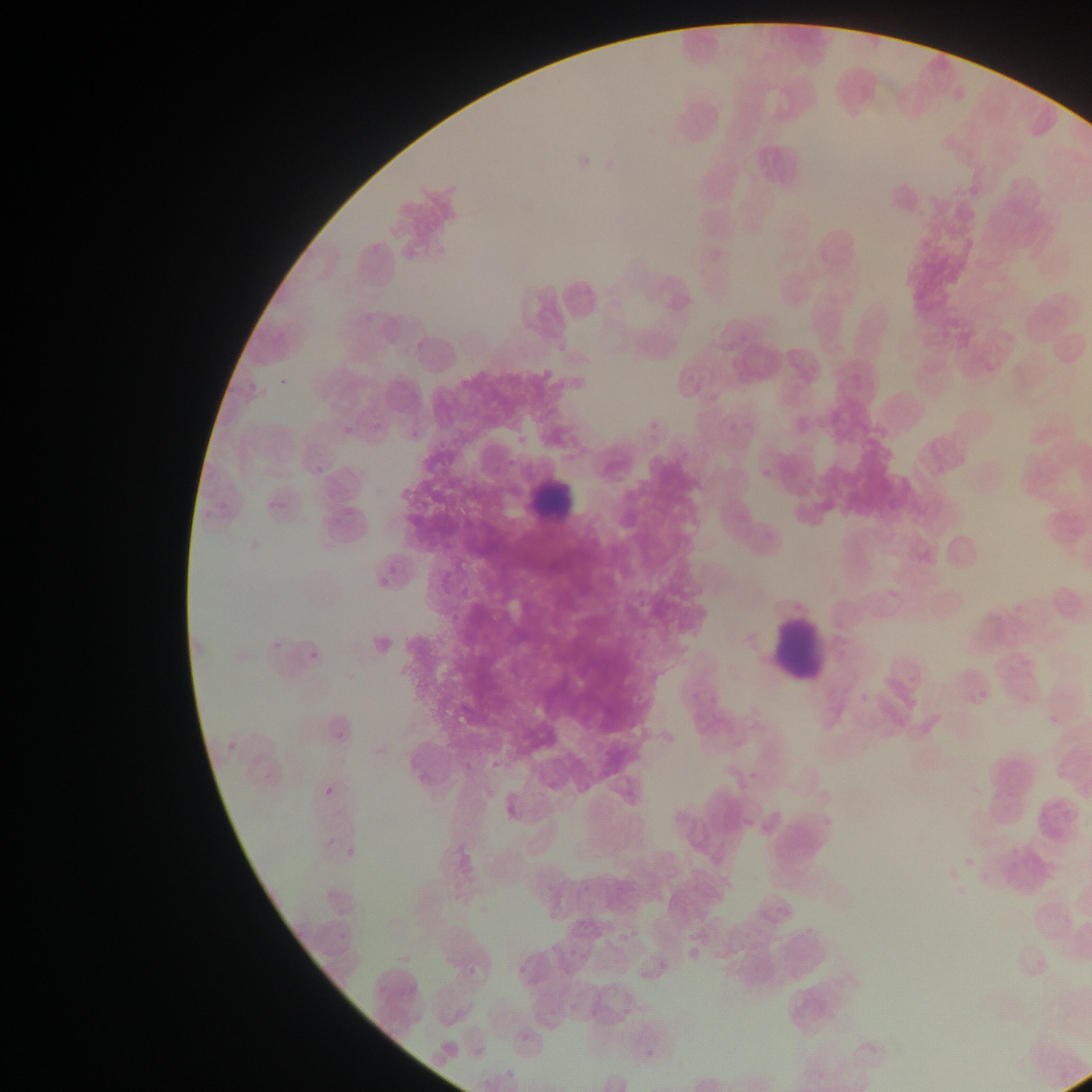 Approximate bounding boxes as [left, top, right, bottom] in pixels. Leukocyte locations: [663, 84, 730, 150], [526, 469, 594, 527], [762, 602, 832, 686]. Malaria parasite locations: [275, 368, 290, 387], [527, 368, 552, 388], [327, 409, 352, 434], [308, 450, 332, 474], [338, 501, 365, 522], [372, 571, 396, 584], [260, 630, 283, 656], [306, 635, 326, 665], [222, 744, 235, 757], [322, 784, 337, 801], [737, 804, 760, 830], [339, 838, 360, 859], [465, 959, 476, 978], [639, 1047, 663, 1061]. One field of view. Image is 1092×1092 pixels. Thin blood film. Mobile-phone photograph taken through the microscope. Collected in Ghana.